Assess the morphology of the erythrocytes.
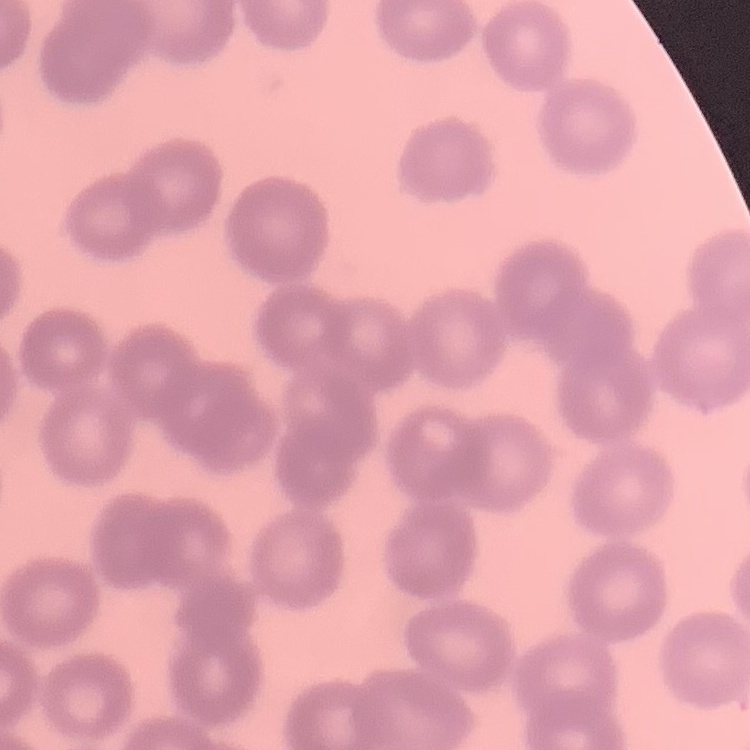
They show no rouleaux formation.

One tile cut from a larger photomicrograph. Field's or Giemsa stain. Thin blood film.